Assess the morphology of the red blood cells.
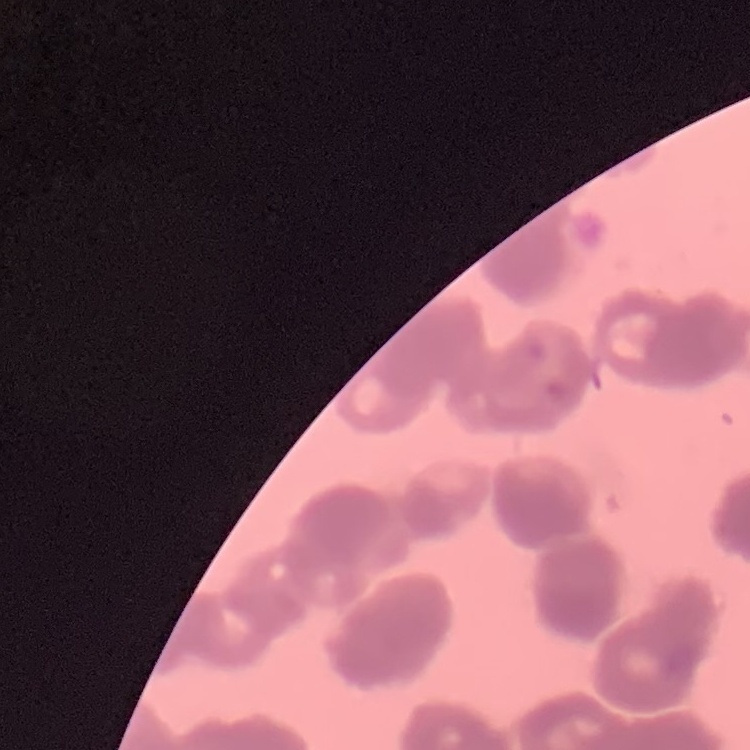

Rouleaux formation.

Summary:
  - Stain: Field's or Giemsa
  - Preparation: thin blood smear
  - Image type: square crop of a larger photomicrograph